Identify the cell.
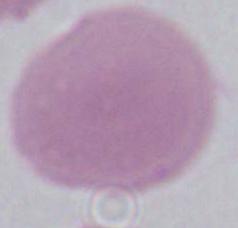
This is an erythrocyte.

Photomicrograph. Captured at 1000x magnification.